Report the malaria status of this cell.
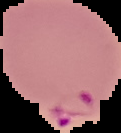

Parasitized.

Summary:
  - Image type: segmented cell region with the area outside set to black
  - Image size: 121×133 pixels
  - Preparation: thin blood smear